Report the malaria status of this cell.
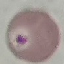

Uninfected.

capture = smartphone through the microscope eyepiece
preparation = thin smear
stain = Giemsa
image type = automatically extracted cell patch, resized to 64 × 64 pixels